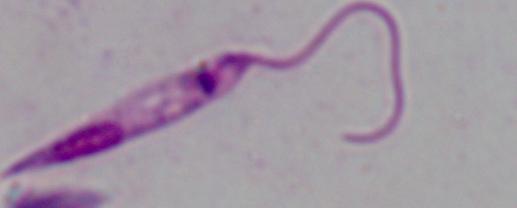

{
  "identification": "Leishmania",
  "modality": "micrograph",
  "magnification": "1000x"
}